Assess for malaria.
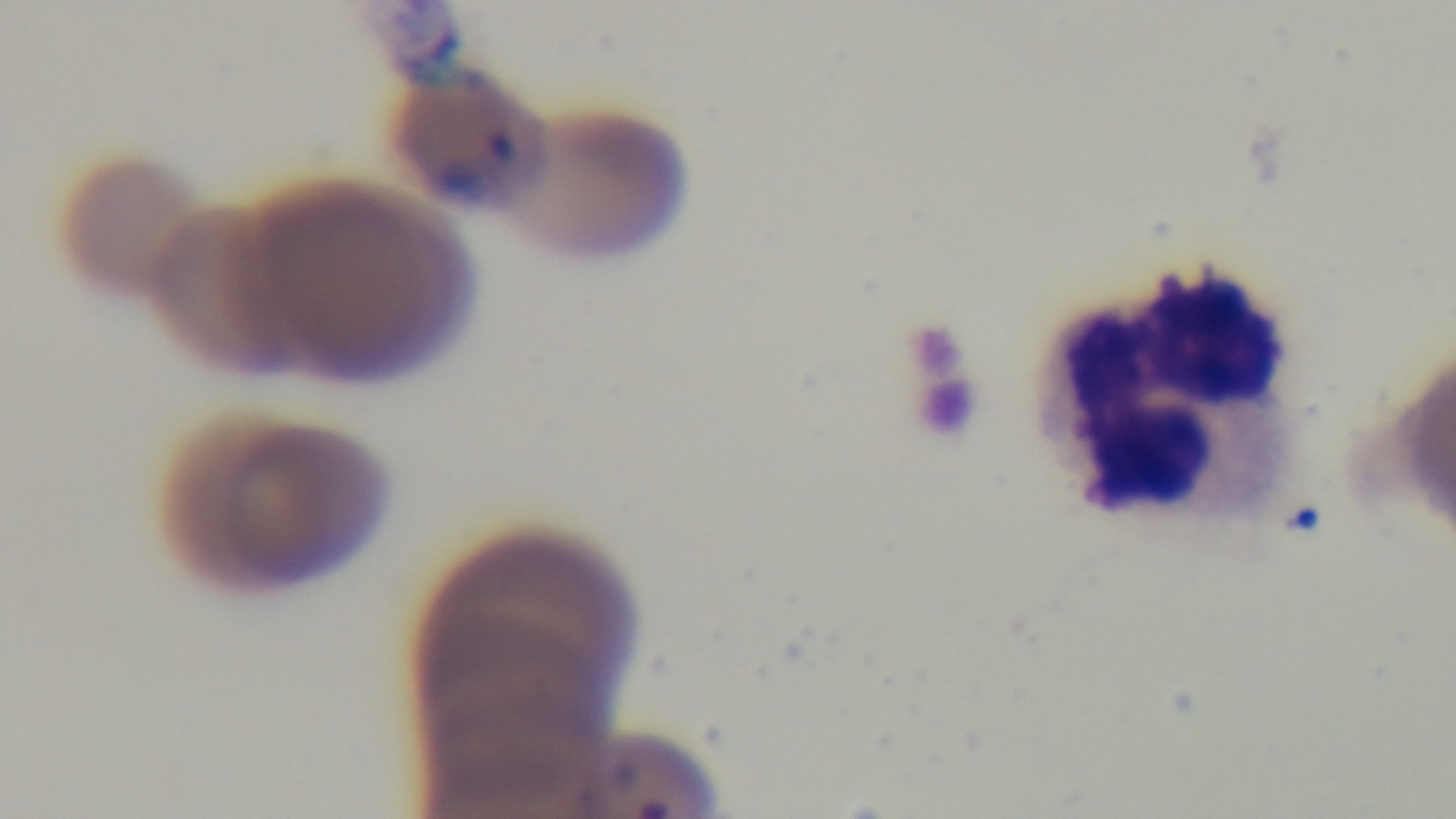
Positive.

modality: light microscopy
capture: mounted 4K digital camera
preparation: thin
stain: Giemsa
objective: 100x oil immersion
field_of_view: single